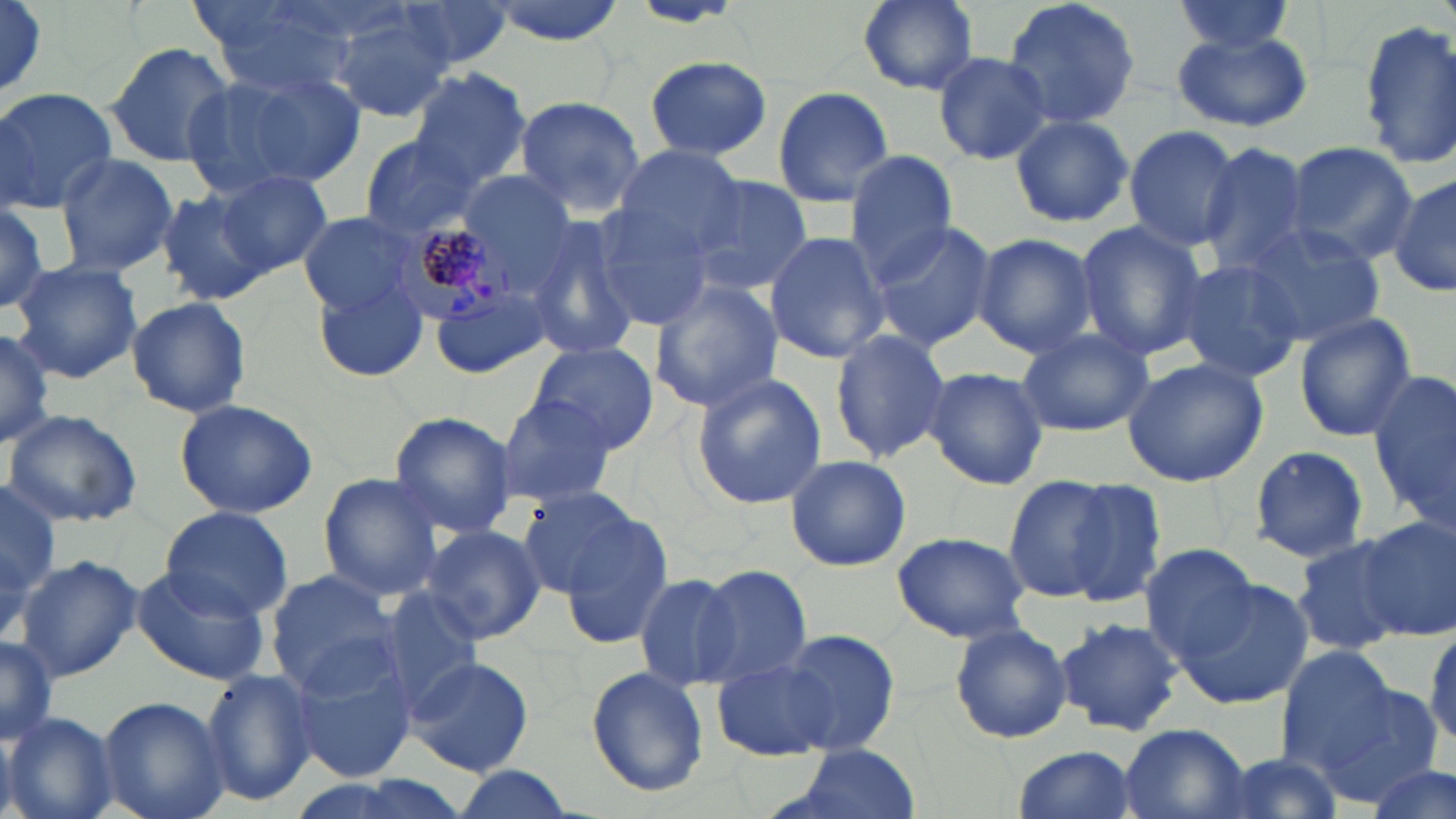

Approximate bounding boxes as named x1/y1/x2/y2 corners in pixels. Uninfected red blood cell locations: (x1=0, y1=0, x2=50, y2=103), (x1=390, y1=0, x2=516, y2=70), (x1=486, y1=0, x2=629, y2=44), (x1=853, y1=0, x2=984, y2=96), (x1=1002, y1=0, x2=1141, y2=132), (x1=1168, y1=0, x2=1299, y2=58), (x1=199, y1=2, x2=358, y2=95), (x1=0, y1=3, x2=50, y2=94), (x1=326, y1=9, x2=455, y2=121), (x1=1355, y1=21, x2=1456, y2=168), (x1=1172, y1=30, x2=1312, y2=134), (x1=105, y1=40, x2=236, y2=171), (x1=932, y1=50, x2=1053, y2=165), (x1=642, y1=57, x2=776, y2=163), (x1=186, y1=67, x2=363, y2=196), (x1=407, y1=69, x2=533, y2=192), (x1=771, y1=86, x2=894, y2=208), (x1=0, y1=87, x2=116, y2=212), (x1=511, y1=95, x2=647, y2=218), (x1=1008, y1=115, x2=1133, y2=229), (x1=1123, y1=125, x2=1242, y2=250), (x1=357, y1=135, x2=482, y2=238), (x1=1280, y1=142, x2=1420, y2=263), (x1=1195, y1=144, x2=1314, y2=275), (x1=612, y1=145, x2=744, y2=260), (x1=843, y1=152, x2=957, y2=280), (x1=54, y1=155, x2=180, y2=276), (x1=456, y1=168, x2=578, y2=280), (x1=213, y1=171, x2=331, y2=274), (x1=1390, y1=172, x2=1456, y2=299), (x1=685, y1=175, x2=813, y2=298), (x1=155, y1=189, x2=273, y2=306), (x1=0, y1=198, x2=56, y2=314), (x1=584, y1=200, x2=716, y2=329), (x1=298, y1=214, x2=421, y2=315), (x1=524, y1=216, x2=641, y2=363), (x1=869, y1=221, x2=998, y2=352), (x1=1074, y1=222, x2=1209, y2=363), (x1=1234, y1=222, x2=1387, y2=345), (x1=764, y1=231, x2=889, y2=361), (x1=972, y1=233, x2=1100, y2=357), (x1=1174, y1=258, x2=1305, y2=384), (x1=8, y1=260, x2=144, y2=384), (x1=311, y1=275, x2=430, y2=383), (x1=647, y1=278, x2=782, y2=412), (x1=430, y1=283, x2=554, y2=377), (x1=126, y1=295, x2=252, y2=419), (x1=1295, y1=315, x2=1417, y2=441), (x1=0, y1=323, x2=53, y2=451), (x1=1016, y1=328, x2=1153, y2=438), (x1=829, y1=329, x2=952, y2=465), (x1=959, y1=338, x2=1097, y2=460), (x1=529, y1=341, x2=660, y2=454), (x1=1121, y1=356, x2=1268, y2=487), (x1=924, y1=367, x2=1048, y2=491), (x1=1371, y1=371, x2=1456, y2=535), (x1=689, y1=372, x2=829, y2=508), (x1=495, y1=396, x2=620, y2=507), (x1=173, y1=397, x2=319, y2=519), (x1=4, y1=409, x2=144, y2=528), (x1=388, y1=411, x2=517, y2=539), (x1=1248, y1=444, x2=1371, y2=566), (x1=784, y1=453, x2=911, y2=571), (x1=317, y1=473, x2=445, y2=600), (x1=1002, y1=473, x2=1151, y2=609), (x1=1, y1=477, x2=60, y2=604), (x1=515, y1=485, x2=645, y2=599), (x1=549, y1=498, x2=672, y2=636), (x1=158, y1=507, x2=294, y2=619), (x1=1357, y1=517, x2=1455, y2=640), (x1=420, y1=523, x2=546, y2=646), (x1=891, y1=531, x2=1031, y2=643), (x1=1291, y1=534, x2=1411, y2=656), (x1=1139, y1=543, x2=1265, y2=664), (x1=16, y1=554, x2=142, y2=681), (x1=130, y1=565, x2=270, y2=687), (x1=692, y1=565, x2=810, y2=687), (x1=264, y1=571, x2=406, y2=702), (x1=633, y1=572, x2=740, y2=690), (x1=1170, y1=575, x2=1316, y2=711), (x1=372, y1=590, x2=483, y2=716), (x1=1055, y1=615, x2=1183, y2=738), (x1=949, y1=622, x2=1072, y2=743), (x1=778, y1=629, x2=901, y2=754), (x1=0, y1=635, x2=59, y2=748), (x1=1276, y1=644, x2=1395, y2=765), (x1=290, y1=648, x2=419, y2=785), (x1=405, y1=656, x2=535, y2=776), (x1=711, y1=656, x2=839, y2=762), (x1=586, y1=666, x2=709, y2=796), (x1=199, y1=669, x2=318, y2=805), (x1=1314, y1=681, x2=1443, y2=807), (x1=99, y1=696, x2=229, y2=819), (x1=2, y1=712, x2=121, y2=819), (x1=1119, y1=725, x2=1250, y2=819), (x1=778, y1=743, x2=926, y2=819), (x1=1010, y1=744, x2=1137, y2=819), (x1=1210, y1=750, x2=1344, y2=817), (x1=1367, y1=761, x2=1453, y2=819), (x1=451, y1=767, x2=576, y2=819). Plasmodium malariae-infected red blood cell locations: (x1=388, y1=219, x2=523, y2=329). Slide-level diagnosis: Plasmodium malariae. Light microscopy. 1000x magnification. Image is 1456×819 pixels. May-Grünwald-Giemsa-stained preparation. One field of a larger specimen. Thin blood film.